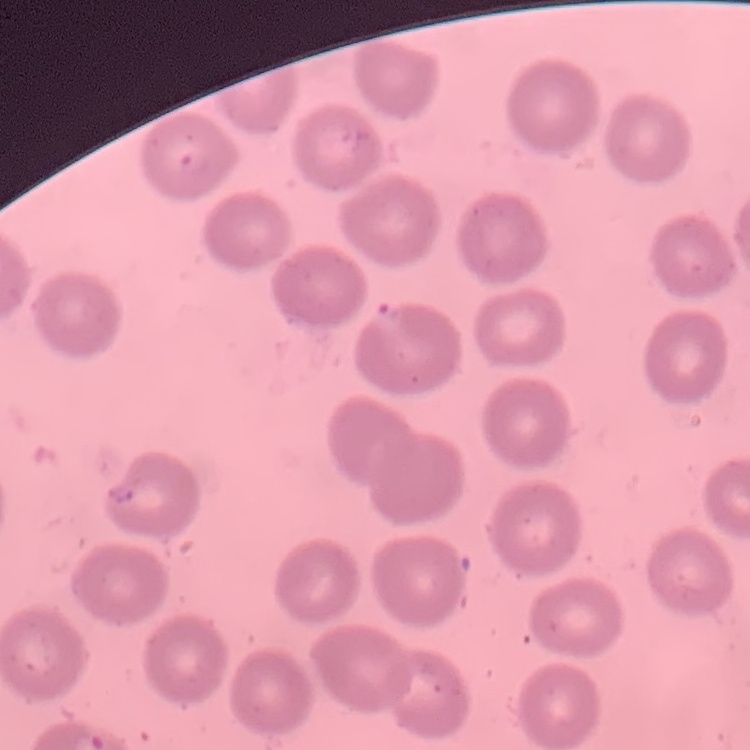
{
  "red_blood_cell_morphology": "no rouleaux formation",
  "stain": "Field's or Giemsa",
  "image_type": "square crop of a larger photomicrograph",
  "preparation": "thin blood film"
}